Give the extent of all uninfected red blood cells.
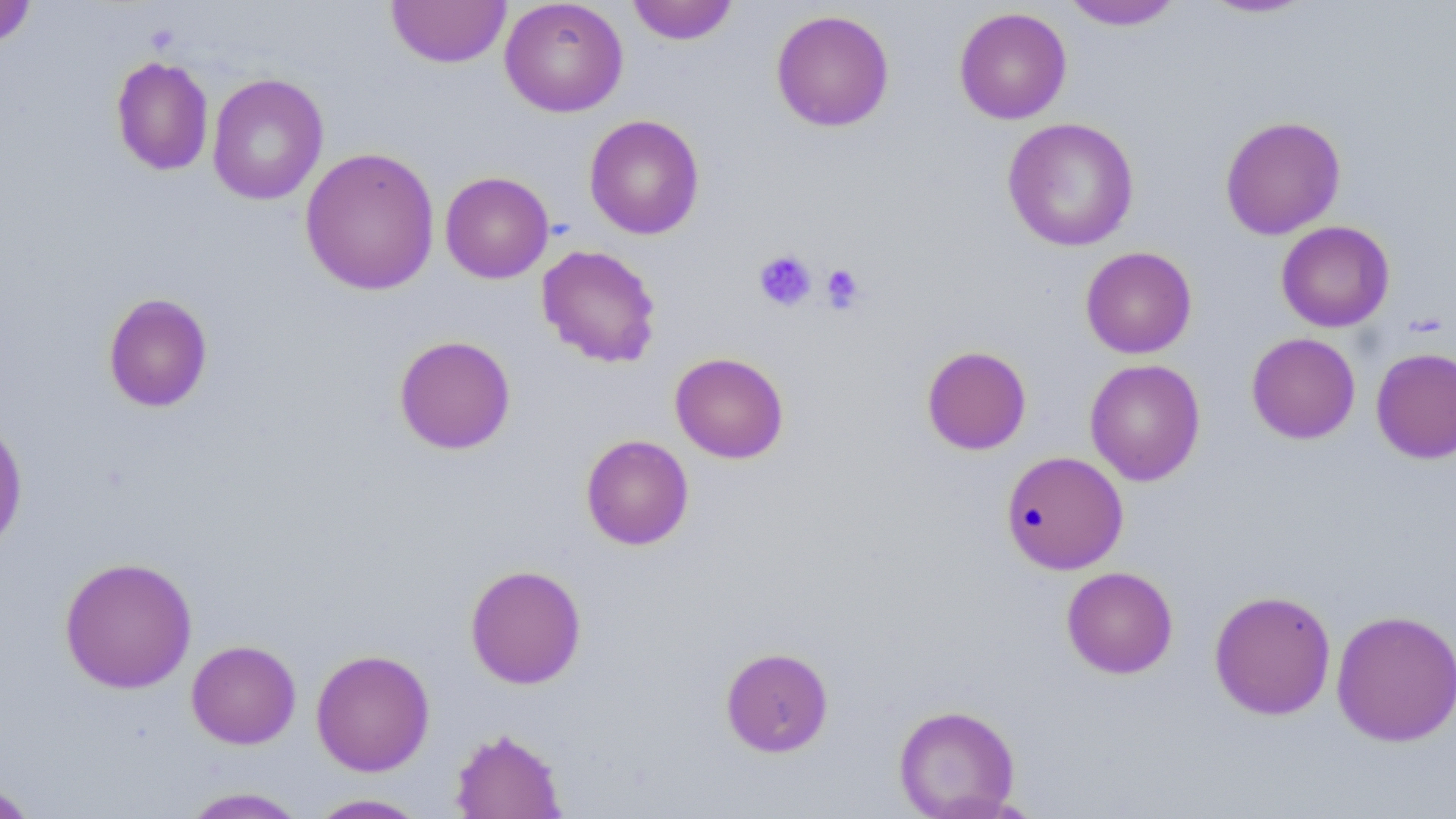
Approximate bounding boxes as [x1, y1, x2, y2] in pixels.
Uninfected red blood cells: [386, 0, 511, 68], [499, 0, 628, 117], [627, 0, 739, 45], [1198, 0, 1319, 19], [0, 1, 38, 51], [1060, 1, 1186, 31], [953, 7, 1072, 125], [770, 9, 894, 133], [110, 55, 215, 177], [207, 73, 328, 206], [584, 114, 704, 240], [1220, 115, 1346, 240], [1002, 116, 1140, 252], [299, 146, 440, 296], [439, 171, 554, 283], [1276, 221, 1395, 332], [536, 244, 661, 368], [1080, 246, 1197, 359], [102, 292, 213, 413], [1246, 332, 1361, 444], [393, 334, 516, 455], [921, 345, 1031, 455], [1371, 347, 1456, 464], [670, 352, 789, 463], [1085, 358, 1205, 486], [0, 416, 28, 556], [580, 434, 694, 550], [1001, 450, 1128, 575], [59, 555, 198, 694], [465, 564, 587, 689], [1061, 566, 1178, 679], [1209, 589, 1337, 720], [1331, 609, 1456, 746], [186, 639, 301, 749], [720, 646, 834, 757], [311, 648, 435, 776], [893, 704, 1021, 818], [450, 727, 566, 818], [0, 781, 40, 818], [179, 786, 308, 818], [307, 794, 430, 818].

Platelet locations: [753, 249, 817, 311], [820, 264, 865, 312]. Slide-level diagnosis: no evidence of blood parasites. 1000x magnification. Thin blood film. Light microscopy. Image is 1456×819 pixels. May-Grünwald-Giemsa stain. One field of a larger specimen.